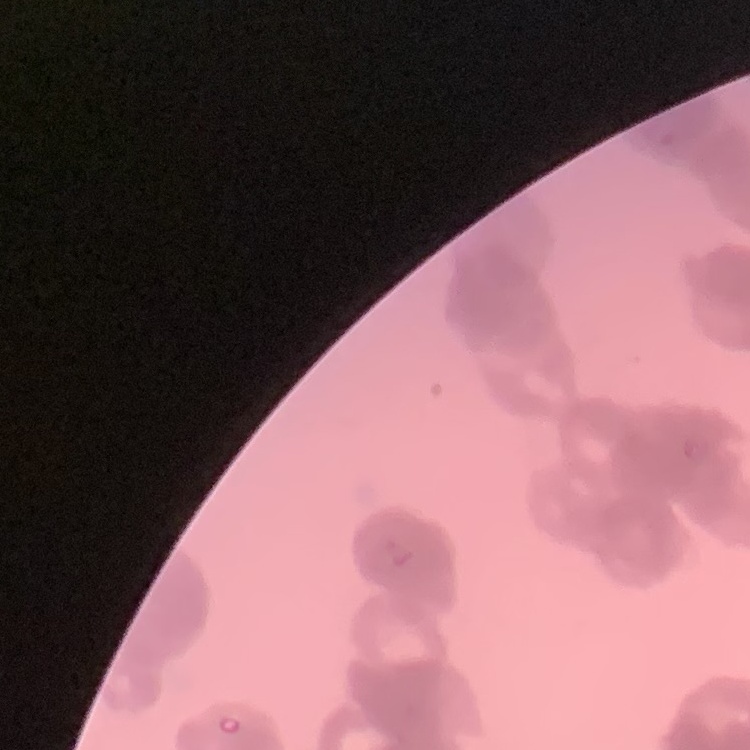

Summary:
  - Erythrocyte morphology: rouleaux formation
  - Stain: Field's or Giemsa
  - Image type: square crop of a larger photomicrograph
  - Preparation: thin peripheral smear